Assess the morphology of the red blood cells.
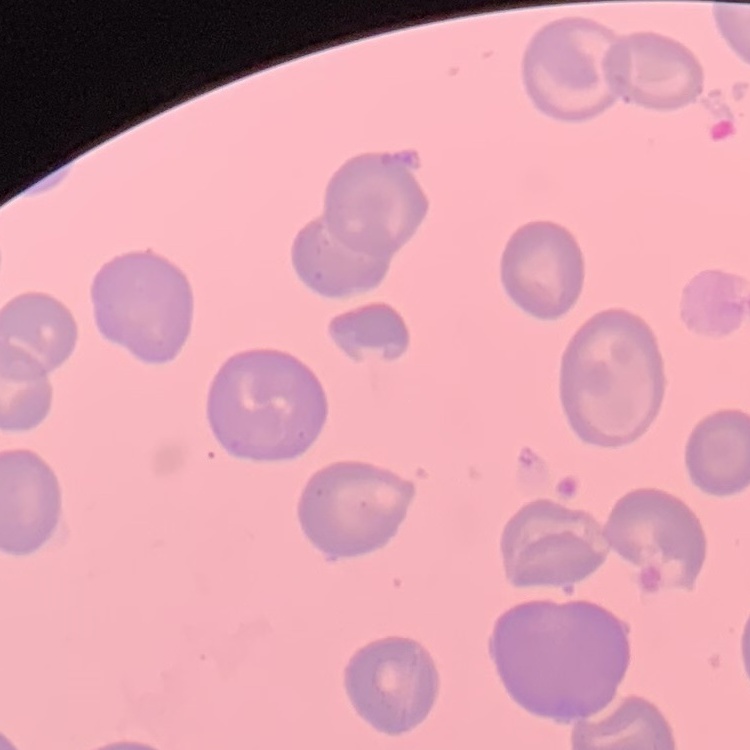

They show no rouleaux formation.

One tile cut from a larger photomicrograph. Field's or Giemsa stain. Thin peripheral smear.